Identify the cell.
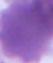

An erythrocyte.

Summary:
  - Modality: micrograph
  - Magnification: 1000x